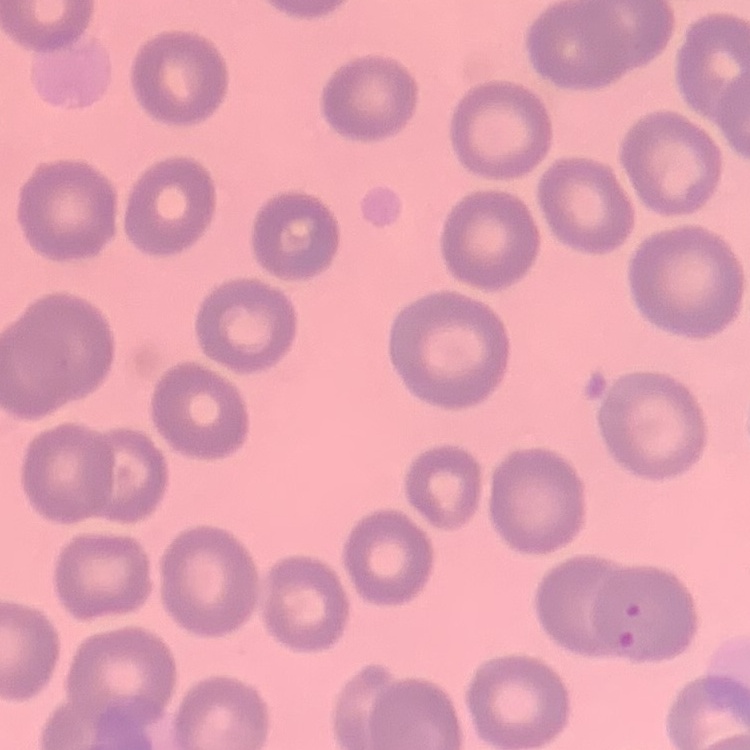
erythrocyte morphology = no rouleaux formation
stain = Field's or Giemsa
image type = one tile cut from a larger photomicrograph
preparation = thin peripheral smear